Assess the morphology of the red blood cells.
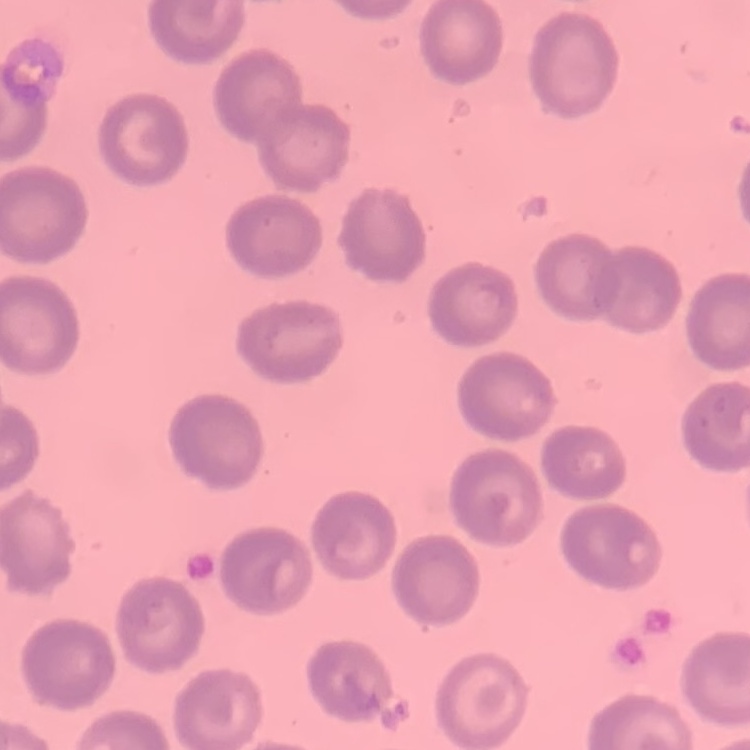
They show no rouleaux formation.

Stained with either Field's or Giemsa. Thin blood smear. One tile cut from a larger photomicrograph.